Assess this cell for malaria.
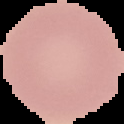

Uninfected.

From a thin blood film. Image is 124×124 pixels. The area outside the segmented cell region is set to black.